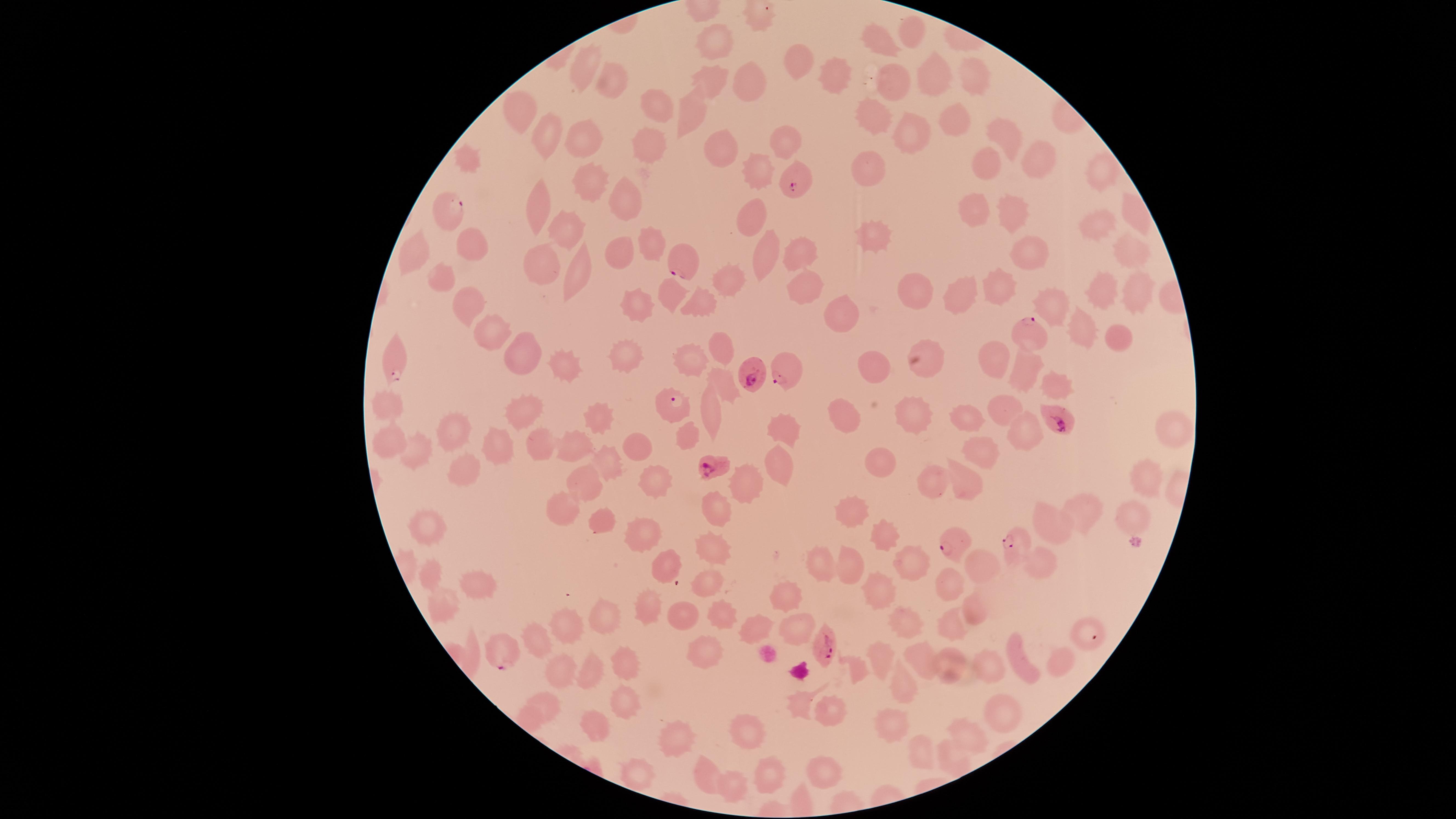
stain = Giemsa
field of view = single
visible region = circular
preparation = thin blood smear
capture = smartphone photograph through the microscope eyepiece
species = Plasmodium falciparum
image size = 1456×819 pixels
parasitized RBCs = approximate marker points as (x, y) in pixels: (793, 182), (456, 214), (685, 262), (1027, 329), (398, 362), (753, 374), (785, 374), (674, 407), (1062, 419), (710, 463), (1015, 543), (953, 545), (828, 645), (501, 650)
presence = malaria parasites seen
uninfected RBCs = approximate marker points as (x, y) in pixels: (914, 34), (883, 40), (720, 43), (801, 65), (586, 73), (973, 75), (929, 76), (833, 77), (716, 79), (895, 83), (746, 84), (615, 85), (653, 106), (694, 109), (521, 110), (955, 119), (874, 120), (911, 133), (1004, 135), (548, 138), (786, 139), (581, 142), (650, 143), (723, 148), (1032, 155), (994, 164), (873, 173), (757, 177), (1104, 177), (589, 178), (636, 195), (539, 210), (978, 213), (1015, 213), (1137, 213), (752, 216), (1099, 223), (571, 227), (878, 238), (655, 244), (478, 247), (769, 251), (1134, 251), (626, 253), (1032, 254), (421, 255), (801, 256), (542, 268), (440, 276), (582, 277), (915, 283), (731, 285), (1000, 287), (1096, 289), (807, 291), (967, 294), (676, 295), (465, 299), (1057, 300), (639, 304), (698, 305), (844, 312), (1079, 327), (487, 331), (1123, 333), (719, 346), (626, 352), (524, 354), (996, 355), (924, 356), (695, 359), (560, 362), (880, 364), (1028, 369), (1061, 380), (725, 387), (387, 402), (712, 407), (526, 409), (1005, 411), (599, 416), (845, 416), (975, 416), (914, 419), (783, 431), (454, 433), (1168, 434), (1028, 435), (687, 437), (637, 446), (539, 447), (391, 448), (980, 449), (569, 451), (418, 452), (494, 453), (605, 463), (879, 463), (771, 468), (462, 472), (968, 477), (654, 481), (1143, 482), (745, 484), (931, 485), (583, 486), (718, 506), (1085, 509), (563, 510), (857, 515), (1130, 516), (1048, 525), (605, 526), (641, 530), (426, 531), (886, 542), (717, 543), (846, 560), (657, 562), (1037, 563), (909, 564), (818, 566), (989, 568), (435, 579), (951, 579), (711, 582), (889, 582), (483, 588), (786, 598), (444, 606), (645, 613), (683, 614), (603, 617), (971, 617), (724, 618), (909, 620), (951, 622), (566, 624), (756, 630), (794, 631), (1083, 633), (539, 642), (707, 654), (878, 658), (917, 659), (1015, 660), (624, 663), (986, 665), (951, 666), (1051, 666), (559, 668), (593, 672), (898, 683), (623, 704), (545, 707), (833, 718), (997, 718), (598, 727), (893, 727), (748, 733), (970, 735), (675, 741), (919, 752), (951, 756), (633, 771), (773, 773), (821, 773), (707, 774), (741, 787)